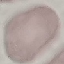
Summary:
  - Result: no malaria parasites detected
  - Image type: automatically extracted cell patch, resized to 64 × 64 pixels
  - Stain: Giemsa
  - Capture: smartphone camera at the microscope eyepiece
  - Preparation: thin smear